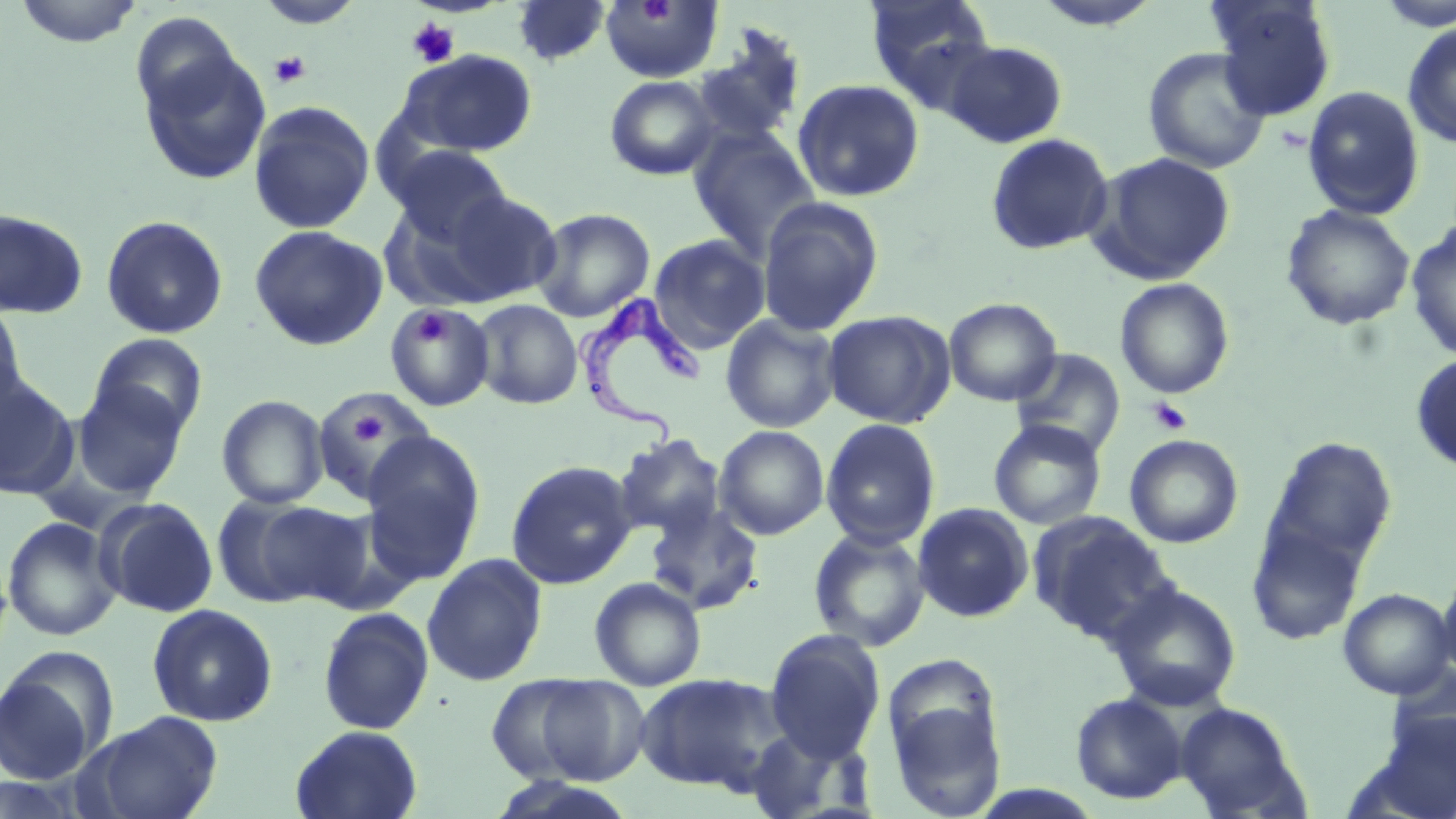
slide-level diagnosis = Trypanosoma brucei
stain = May-Grünwald-Giemsa
field of view = one of a larger specimen
uninfected red blood cell locations = approximate bounding boxes as (x1, y1, x2, y2) in pixels: (12, 0, 146, 48), (255, 0, 365, 30), (511, 0, 613, 67), (864, 0, 997, 103), (1029, 0, 1164, 31), (1208, 0, 1338, 120), (600, 1, 723, 84), (1374, 1, 1456, 32), (130, 11, 243, 121), (1402, 22, 1456, 148), (691, 25, 808, 147), (942, 40, 1067, 148), (138, 44, 271, 185), (1142, 47, 1271, 174), (399, 48, 538, 158), (604, 75, 721, 181), (792, 79, 924, 202), (1302, 85, 1425, 221), (248, 100, 376, 234), (688, 126, 821, 261), (985, 133, 1115, 255), (388, 145, 513, 248), (1088, 151, 1236, 285), (416, 189, 564, 307), (757, 196, 885, 337), (1280, 204, 1416, 330), (532, 207, 655, 322), (0, 208, 88, 319), (100, 215, 228, 339), (1405, 221, 1456, 362), (249, 225, 387, 351), (648, 234, 770, 352), (1114, 278, 1235, 399), (943, 297, 1062, 406), (472, 299, 583, 410), (0, 301, 27, 417), (385, 302, 496, 412), (822, 309, 956, 428), (720, 314, 841, 433), (89, 334, 208, 436), (1010, 348, 1126, 458), (1410, 353, 1456, 474), (0, 378, 77, 499), (72, 379, 189, 499), (311, 385, 435, 503), (217, 395, 329, 509), (820, 418, 941, 549), (988, 419, 1106, 530), (714, 425, 830, 540), (359, 431, 486, 584), (612, 433, 727, 539), (1124, 434, 1244, 548), (1261, 436, 1398, 579), (505, 460, 638, 589), (212, 494, 350, 608), (96, 498, 219, 617), (644, 500, 765, 616), (912, 502, 1034, 623), (1029, 511, 1176, 644), (2, 516, 122, 642), (1245, 516, 1367, 647), (808, 527, 930, 652), (422, 553, 547, 687), (1437, 562, 1456, 683), (589, 577, 707, 691), (1106, 580, 1242, 711), (1338, 588, 1455, 699), (147, 604, 278, 727), (317, 606, 434, 735), (764, 629, 886, 763), (0, 659, 109, 786), (1389, 663, 1456, 760), (635, 672, 785, 794), (884, 674, 1009, 819), (486, 675, 601, 783), (531, 675, 651, 784), (1070, 692, 1189, 804), (1173, 701, 1308, 818), (83, 711, 224, 819), (1374, 711, 1456, 819), (290, 724, 423, 819), (744, 726, 873, 819), (487, 776, 638, 818)
image size = 1456×819 pixels
Trypanosoma brucei locations = approximate bounding boxes as (x1, y1, x2, y2) in pixels: (574, 293, 710, 445)
modality = optical microscopy
preparation = thin blood film
platelet locations = approximate bounding boxes as (x1, y1, x2, y2) in pixels: (406, 18, 460, 68), (269, 51, 311, 89), (412, 310, 449, 347), (1148, 396, 1192, 436), (351, 415, 387, 446)
magnification = 1000x